Name the cell type shown.
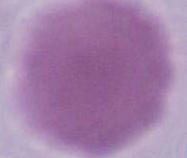
An erythrocyte.

Summary:
  - Magnification: 1000x
  - Modality: micrograph